Describe the morphology of the red blood cells.
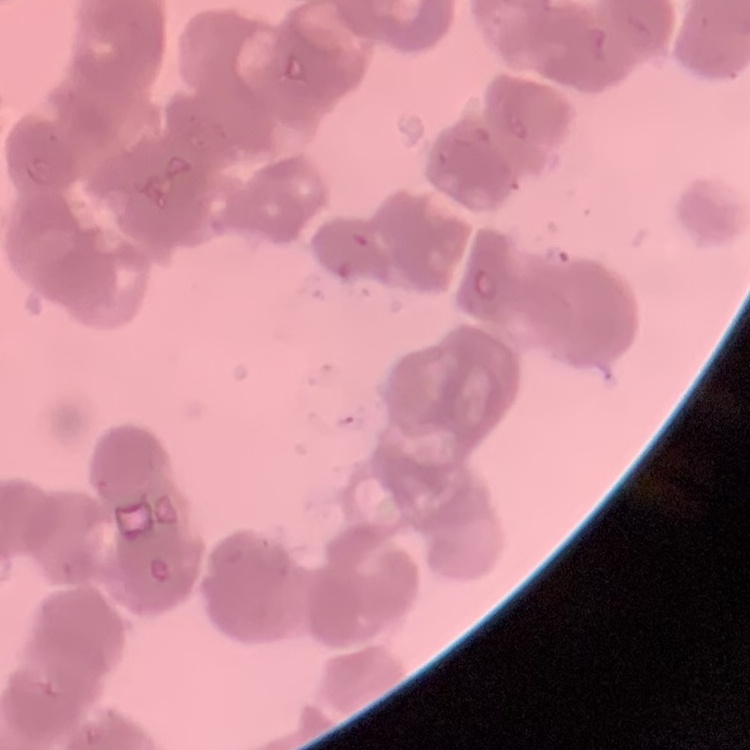

They show rouleaux formation.

Field's or Giemsa stain. Thin blood smear. One tile cut from a larger photomicrograph.